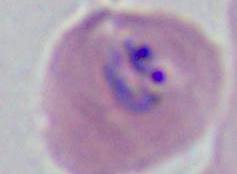

A Plasmodium parasite is seen. Micrograph. Captured at either 400x or 1000x magnification.